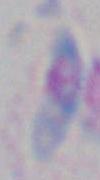

Photomicrograph. Toxoplasma gondii is seen. 1000x magnification.